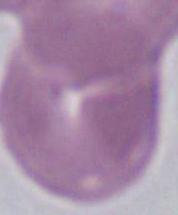 Photomicrograph. A red blood cell is shown. 1000x magnification.